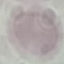
result: no malaria parasites detected
preparation: thin smear
capture: smartphone camera at the microscope eyepiece
stain: Giemsa
image_type: cell patch, automatically extracted from a larger field of view and resized to 64 × 64 pixels